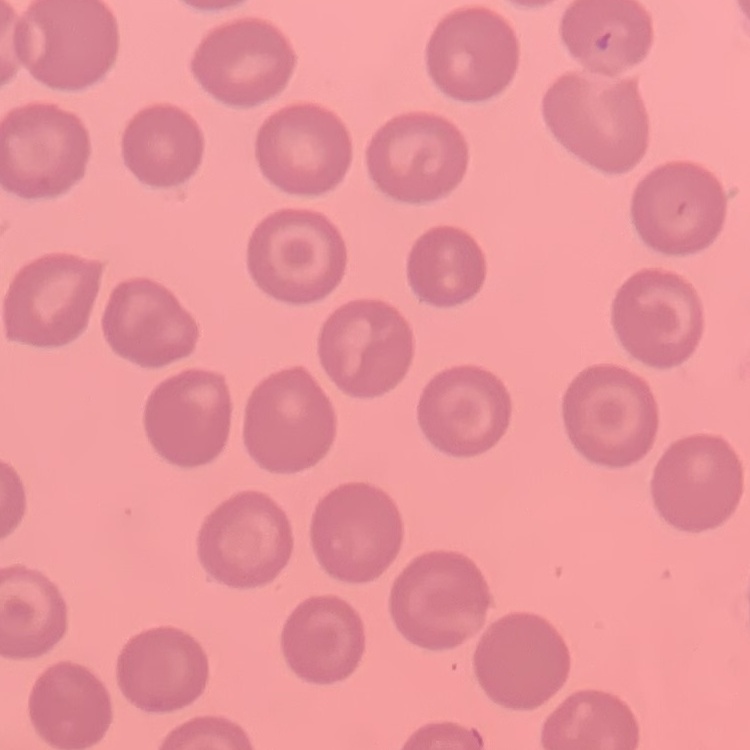
Summary:
  - Erythrocyte morphology: no rouleaux formation
  - Image type: one tile cut from a larger photomicrograph
  - Preparation: thin blood smear
  - Stain: Field's or Giemsa